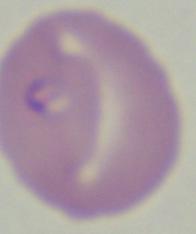
{
  "magnification": "1000x",
  "modality": "photomicrograph",
  "identification": "Babesia"
}